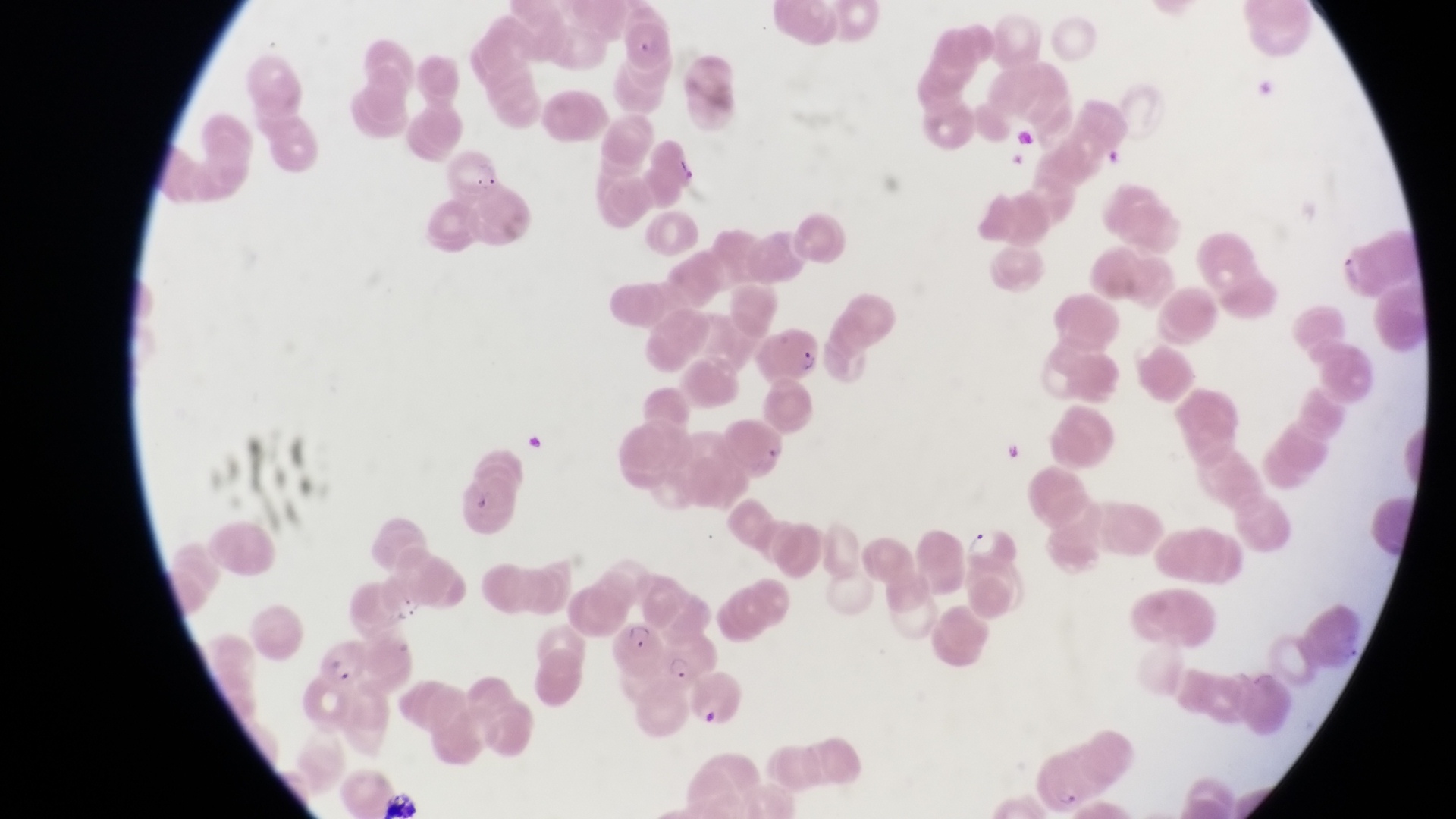

Approximate bounding boxes as left top right bottom in pixels.
Summary:
  - Artifact (platelet-like body, stain precipitate, or debris) locations: 1103 142 1129 169; 465 495 495 519
  - Trophozoite locations: 964 521 1001 558; 666 651 699 684
  - Parasitised red blood cell locations: 752 327 818 386; 605 618 666 676; 317 635 370 690
  - Magnification: 1000x
  - Preparation: thin blood film
  - Image size: 1456×819 pixels
  - Capture: smartphone photograph through the eyepiece of an Olympus CX-23 microscope
  - Country: Uganda
  - Field of view: single